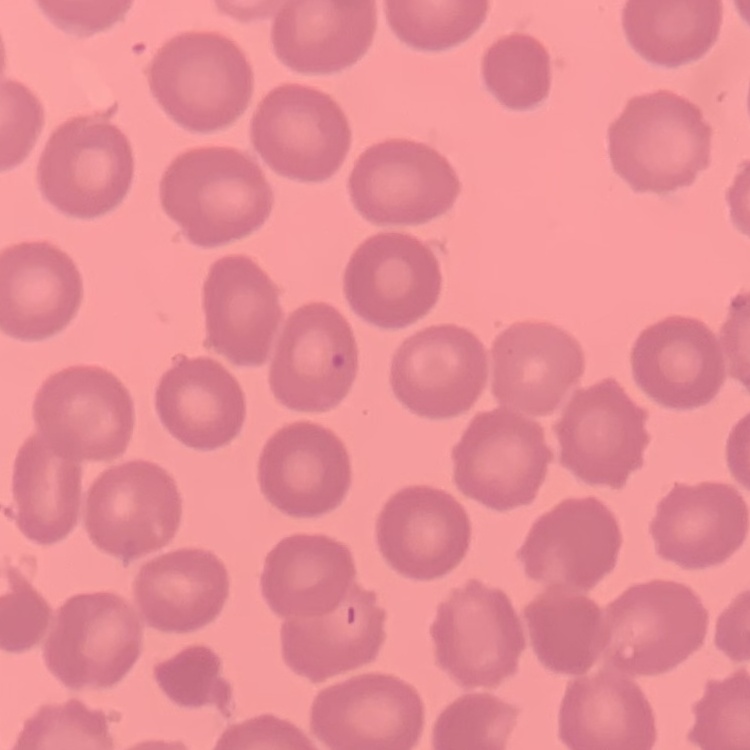 The red blood cells show no rouleaux formation. One tile cut from a larger photomicrograph. Thin blood smear. Stained with either Field's or Giemsa.